Give the position of every Plasmodium parasite.
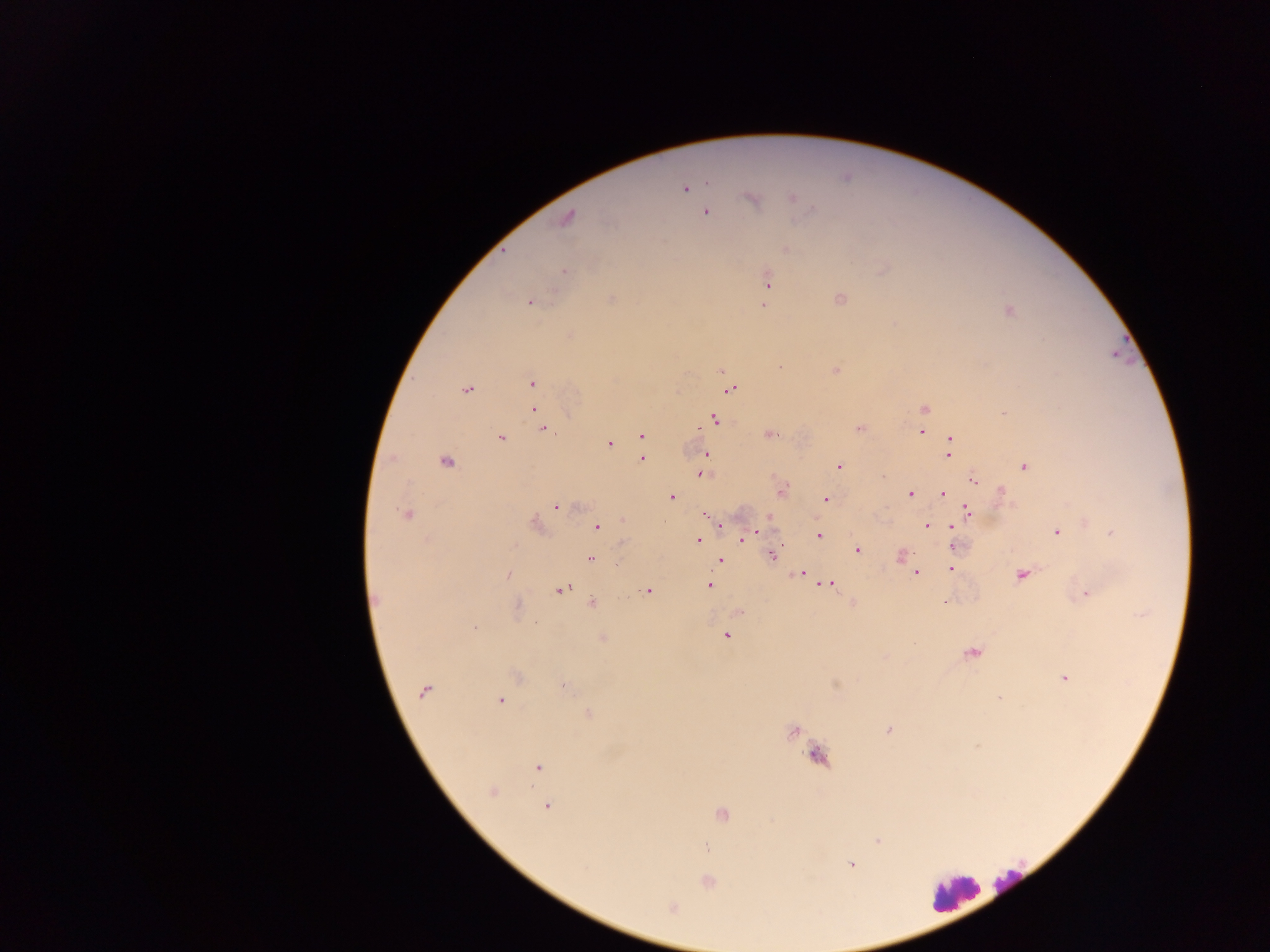
Approximate centers as (x, y) in pixels.
Plasmodium parasites: (685, 189), (792, 198), (753, 199), (706, 213), (566, 218), (786, 250), (564, 271), (768, 281), (840, 299), (611, 300), (530, 302), (763, 305), (1009, 311), (780, 367), (836, 370), (532, 384), (466, 389), (729, 389), (534, 409), (924, 410), (1002, 413), (715, 419), (859, 428), (542, 429), (921, 432), (770, 434), (642, 436), (501, 437), (950, 439), (609, 443), (706, 453), (949, 455), (642, 459), (447, 462), (704, 465), (839, 466), (1024, 467), (702, 474), (974, 482), (781, 491), (1001, 491), (944, 493), (910, 494), (671, 497), (826, 500), (557, 508), (968, 512), (405, 514), (708, 516), (769, 519), (536, 524), (720, 524), (928, 525), (598, 528), (951, 528), (761, 531), (1057, 532), (1111, 533), (751, 535), (819, 536), (745, 537), (698, 540), (952, 546), (858, 549), (772, 555), (901, 556), (591, 559), (720, 561), (951, 569), (916, 572), (801, 573), (509, 574), (1022, 575), (829, 584), (709, 586), (561, 590), (648, 591), (1087, 594), (945, 602), (592, 603), (853, 603), (518, 606), (738, 611), (475, 627), (727, 636), (603, 638), (972, 654), (517, 677), (1065, 678), (565, 686), (424, 691), (999, 698), (501, 700), (589, 715), (793, 731), (890, 731), (977, 745), (818, 757), (538, 768), (492, 792), (547, 806), (721, 815), (878, 841), (707, 847), (851, 865), (708, 882), (671, 908).

preparation = thick blood smear
field of view = single
leukocyte locations = approximate centers as (x, y) in pixels: (1010, 877), (955, 892)
image size = 1270×952 pixels
capture = mobile-phone photograph through a microscope
country = Ghana